Assess this cell for malaria.
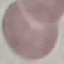
Uninfected.

{
  "capture": "smartphone through the microscope eyepiece",
  "image_type": "cell patch, automatically extracted from a larger field of view and resized to 64 × 64 pixels",
  "preparation": "thin blood smear",
  "stain": "Giemsa"
}